Give the position of every Plasmodium parasite.
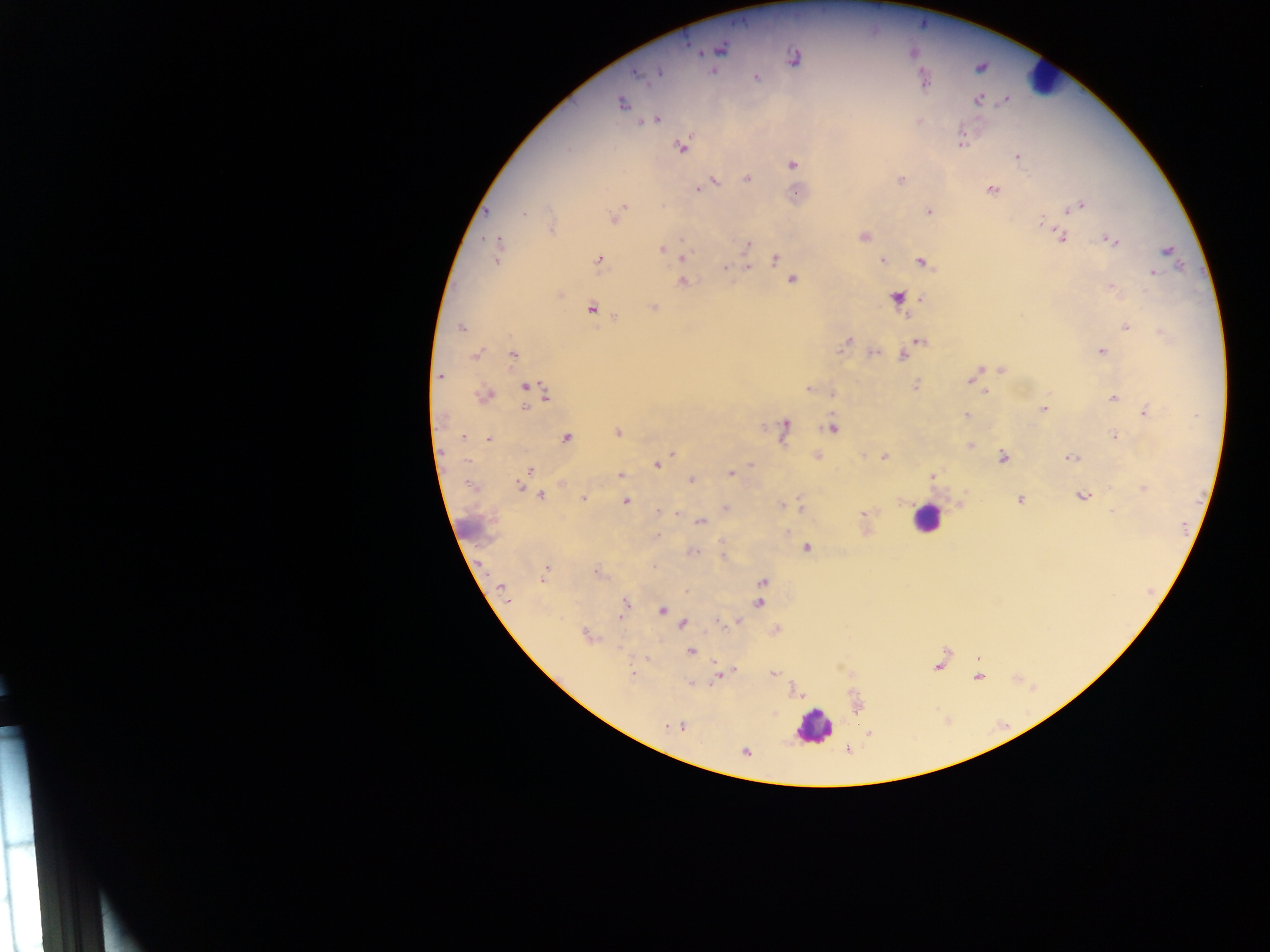
Approximate centers as (x, y) in pixels.
Plasmodium parasites: (686, 42), (721, 49), (696, 53), (795, 56), (659, 72), (636, 74), (757, 76), (924, 79), (978, 99), (624, 103), (657, 119), (962, 144), (680, 147), (1018, 154), (791, 164), (900, 178), (747, 179), (716, 181), (696, 188), (991, 188), (1083, 201), (622, 206), (662, 206), (1069, 209), (488, 211), (929, 211), (526, 213), (618, 214), (613, 218), (1041, 222), (864, 235), (1061, 236), (1104, 237), (1121, 239), (747, 245), (498, 247), (661, 248), (682, 258), (882, 258), (597, 260), (775, 260), (921, 262), (750, 265), (926, 265), (725, 267), (1155, 273), (792, 279), (682, 280), (560, 295), (655, 307), (592, 308), (615, 315), (1125, 327), (463, 328), (847, 338), (920, 341), (842, 344), (1102, 351), (872, 352), (512, 354), (474, 355), (902, 356), (1001, 367), (977, 370), (440, 376), (916, 383), (968, 383), (525, 386), (806, 389), (985, 391), (832, 394), (544, 396), (1113, 398), (1042, 407), (525, 408), (1145, 411), (964, 416), (788, 424), (617, 432), (1113, 435), (464, 437), (567, 438), (488, 440), (818, 455), (883, 455), (666, 456), (1004, 456), (1070, 457), (750, 465), (657, 467), (530, 469), (622, 474), (729, 474), (692, 480), (560, 483), (474, 484), (519, 487), (1141, 487), (1084, 495), (541, 497), (582, 497), (1021, 500), (626, 502), (781, 504), (725, 508), (1113, 511), (657, 512), (862, 513), (700, 520), (657, 535), (721, 542), (805, 547), (692, 551), (723, 555), (547, 571), (598, 572), (544, 577), (763, 582), (501, 586), (687, 592), (758, 603), (625, 604), (624, 610), (661, 611), (737, 621), (684, 624), (718, 624), (584, 633), (692, 651), (631, 672), (773, 673), (716, 678), (690, 682), (684, 726), (746, 752).

Leukocyte locations: (1046, 81), (933, 519), (816, 729). One field of view. Image is 1270×952 pixels. Collected in Ghana. Thick blood film. Photographed through a microscope with a mobile-phone camera.